Comment on the morphology of the erythrocytes.
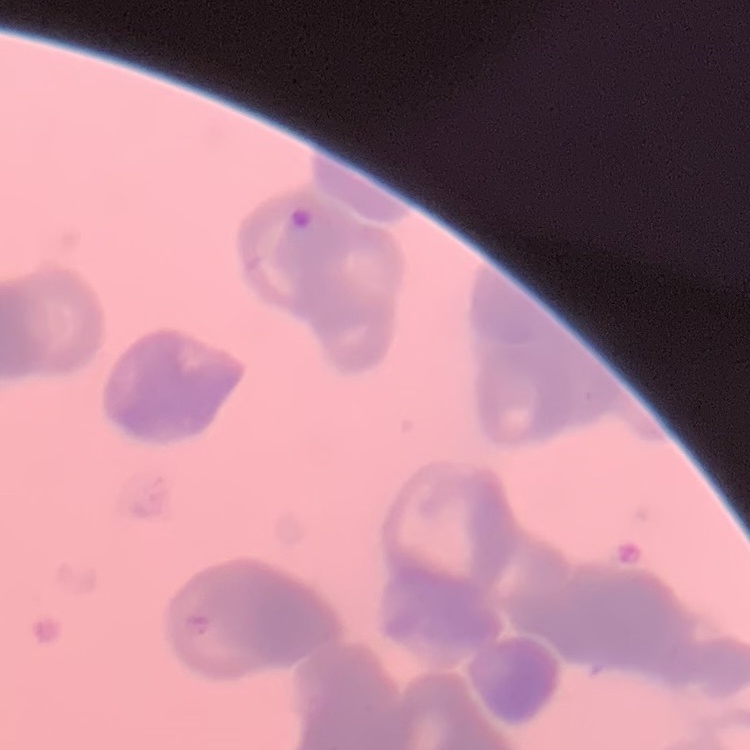
They show rouleaux formation.

Thin peripheral smear. Field's or Giemsa stain. One tile cut from a larger photomicrograph.